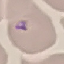
result: no malaria parasites detected
preparation: thin blood smear
stain: Giemsa
image_type: automatically extracted cell patch, resized to 64 × 64 pixels
capture: smartphone through the microscope eyepiece